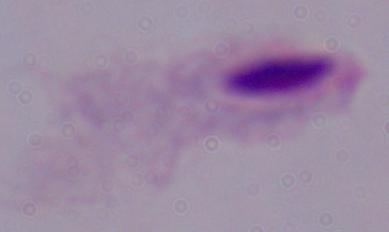 1000x magnification. Micrograph. A trichomonad is shown.